Identify the parasite.
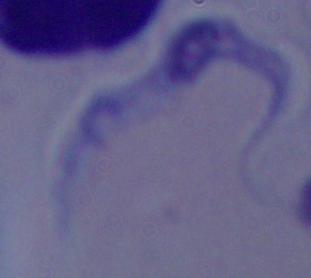
This is a trypanosome.

{
  "modality": "photomicrograph",
  "magnification": "1000x"
}